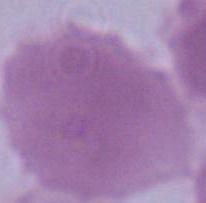
Captured at 1000x magnification. Micrograph. A red blood cell is seen.